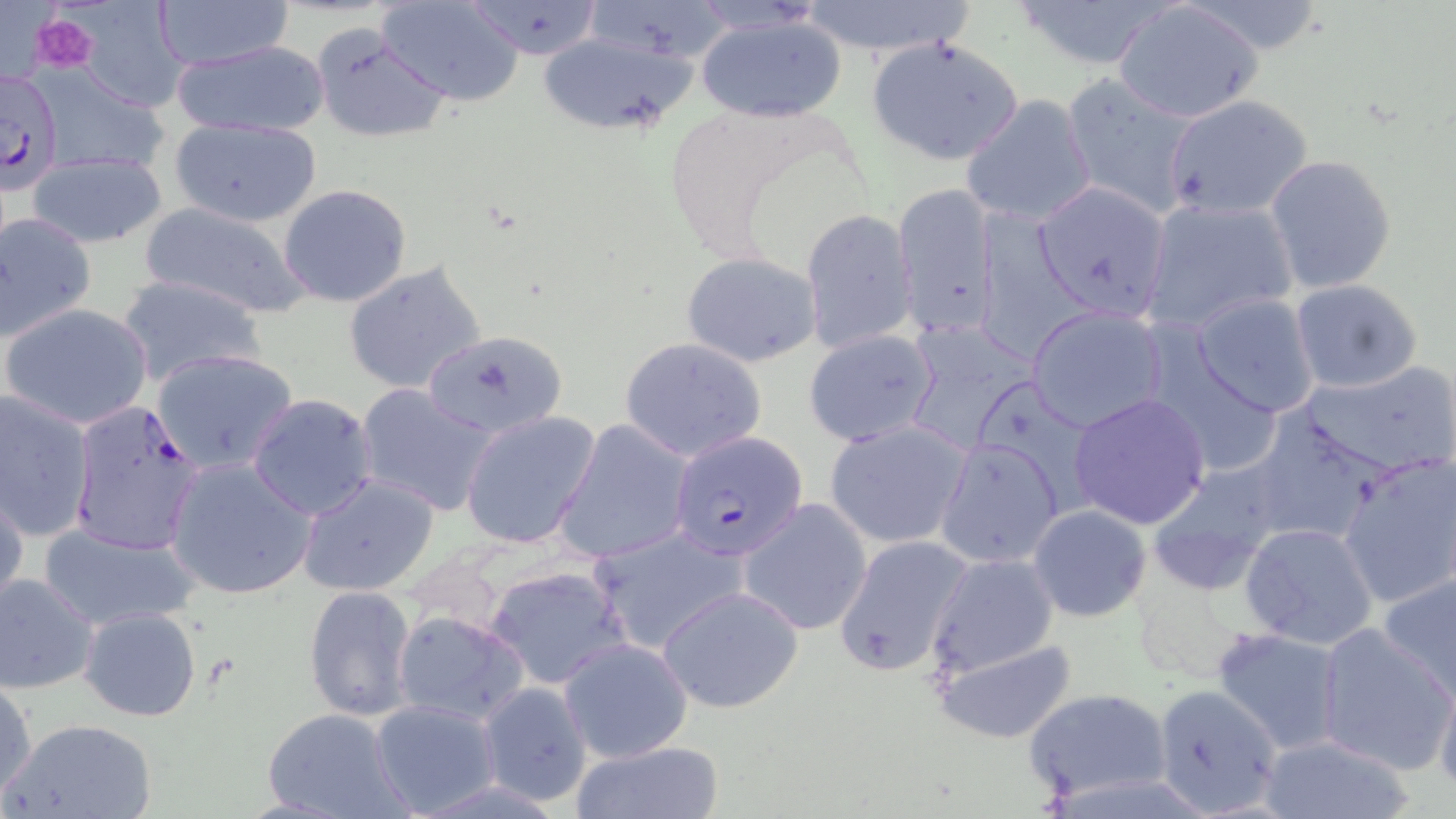
Summary:
  - Coordinate format: approximate bounding boxes as [x1, y1, x2, y2] in pixels
  - Plasmodium falciparum-infected red blood cell locations: [0, 68, 63, 192], [69, 396, 208, 558], [671, 432, 807, 560]
  - Platelet locations: [32, 14, 98, 73]
  - Uninfected red blood cell locations: [70, 0, 192, 113], [377, 0, 526, 105], [461, 0, 608, 59], [582, 0, 742, 66], [1006, 0, 1177, 70], [153, 1, 295, 70], [796, 1, 979, 58], [1115, 2, 1261, 123], [694, 13, 846, 122], [309, 22, 452, 143], [535, 31, 699, 137], [866, 36, 1025, 166], [169, 39, 330, 138], [28, 63, 172, 183], [1057, 72, 1199, 218], [1164, 93, 1313, 219], [960, 94, 1098, 227], [168, 119, 322, 227], [27, 152, 168, 248], [1265, 154, 1397, 294], [1033, 179, 1173, 323], [893, 181, 999, 338], [280, 184, 412, 308], [1140, 196, 1299, 335], [135, 201, 317, 321], [973, 206, 1093, 362], [800, 209, 918, 355], [0, 212, 97, 342], [681, 252, 822, 367], [342, 261, 489, 396], [115, 274, 266, 388], [1290, 278, 1424, 393], [1192, 294, 1321, 417], [2, 302, 154, 430], [1027, 305, 1169, 432], [903, 319, 1037, 455], [803, 328, 939, 448], [422, 329, 569, 437], [619, 336, 771, 463], [152, 347, 300, 474], [1301, 361, 1456, 476], [355, 383, 497, 516], [0, 389, 95, 541], [1068, 392, 1212, 529], [247, 393, 380, 520], [460, 410, 602, 550], [1247, 410, 1390, 548], [553, 419, 695, 565], [825, 420, 972, 549], [935, 437, 1064, 569], [1339, 453, 1456, 609], [164, 458, 317, 601], [1146, 463, 1288, 594], [298, 471, 440, 597], [0, 481, 28, 617], [738, 497, 873, 636], [1027, 505, 1152, 623], [39, 520, 197, 628], [1240, 522, 1381, 652], [588, 524, 749, 654], [832, 535, 972, 678], [924, 553, 1060, 680], [485, 563, 632, 687], [0, 573, 99, 695], [1379, 573, 1456, 698], [302, 584, 418, 725], [659, 585, 804, 713], [78, 606, 202, 722], [393, 610, 530, 725], [1314, 623, 1455, 771], [1212, 628, 1347, 755], [558, 638, 694, 762], [930, 638, 1079, 743], [1431, 673, 1456, 792], [0, 679, 35, 801], [476, 682, 593, 806], [1150, 684, 1284, 816], [1024, 687, 1174, 805], [369, 699, 502, 815], [260, 708, 412, 819], [4, 717, 159, 819], [1258, 733, 1415, 819], [569, 739, 724, 819]
  - Slide-level diagnosis: Plasmodium falciparum
  - Preparation: thin blood smear
  - Field of view: single
  - Modality: optical microscopy
  - Magnification: 1000x
  - Stain: May-Grünwald-Giemsa
  - Image size: 1456×819 pixels